Describe the morphology of the erythrocytes.
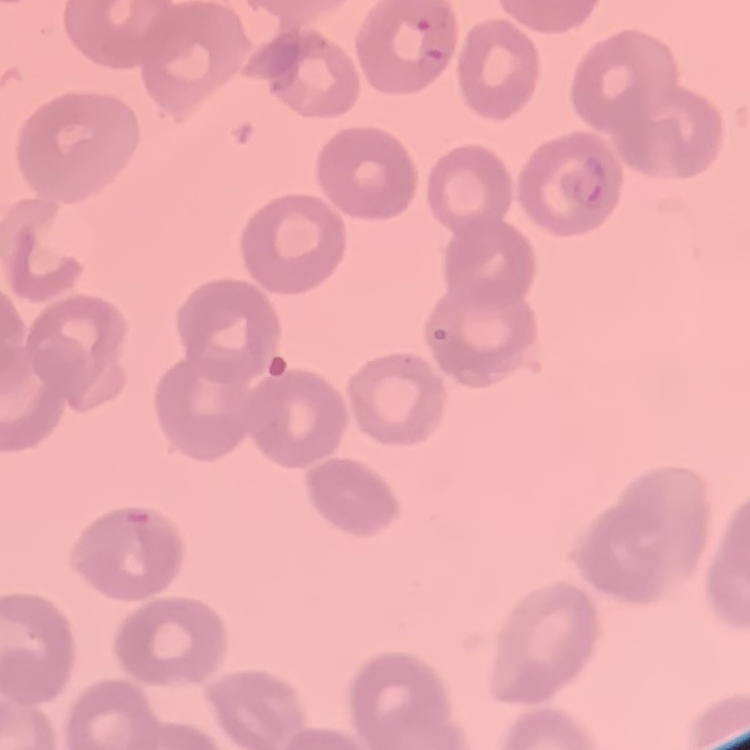

No rouleaux formation.

Field's or Giemsa stain. Square crop of a larger photomicrograph. Thin blood smear.